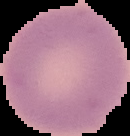 The area outside the segmented cell region is set to black. Result: no malaria parasites seen. Image is 130×136 pixels. From a thin blood film.